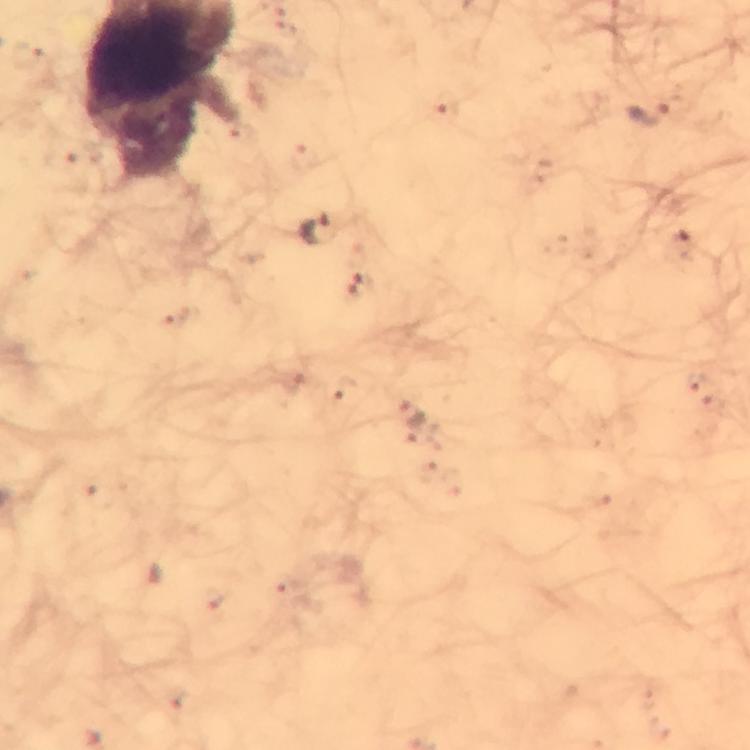

Approximate centers as {x, y} in pixels.
Summary:
  - Plasmodium parasite locations: {650, 114}, {314, 229}, {411, 415}
  - Image size: 750×750 pixels
  - Immersion oil: used
  - Cropped from: one field of view
  - Capture: smartphone mounted on the microscope
  - Stain: Giemsa
  - Preparation: thick blood film
  - Context: from a malaria diagnostic workup
  - Magnification: 100x